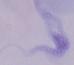

{
  "identification": "trypanosome",
  "magnification": "1000x",
  "modality": "micrograph"
}